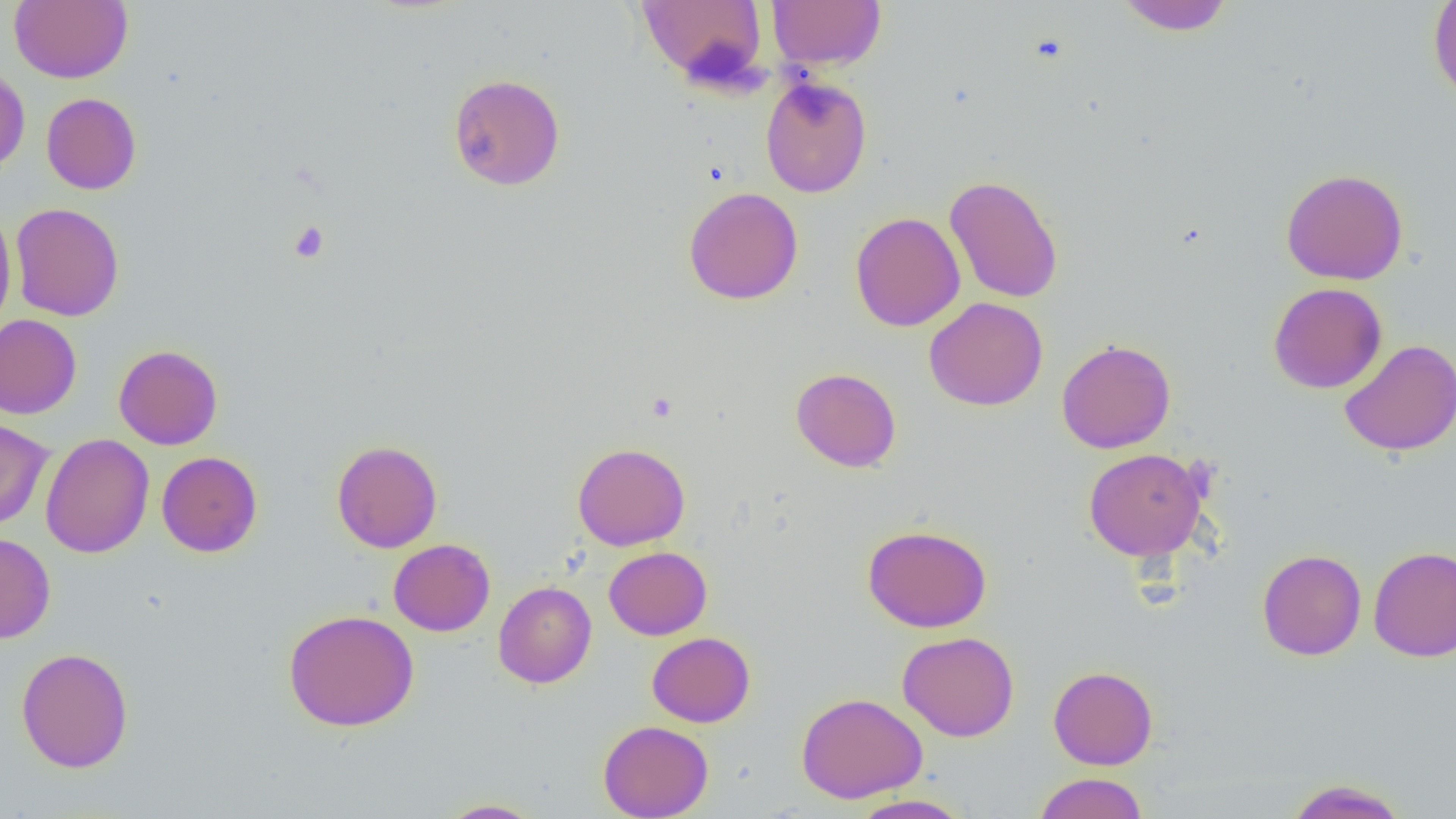
Summary:
  - Coordinate format: approximate bounding boxes as (x1,y1)-(x2,y2) corner pairs in pixels
  - Platelet locations: (289,221)-(329,263), (647,392)-(677,421)
  - Uninfected red blood cell locations: (10,0)-(132,83), (636,0)-(767,85), (767,0)-(886,71), (1115,0)-(1234,35), (1428,0)-(1456,103), (0,65)-(30,176), (447,73)-(565,190), (760,76)-(872,198), (41,92)-(142,194), (1281,168)-(1408,285), (944,174)-(1063,303), (683,186)-(803,305), (10,203)-(124,321), (0,206)-(16,334), (850,212)-(965,332), (1268,282)-(1387,394), (924,297)-(1048,411), (0,314)-(82,419), (1056,339)-(1175,454), (1338,339)-(1456,457), (113,344)-(223,450), (790,367)-(902,472), (0,418)-(53,530), (40,432)-(154,559), (331,439)-(442,553), (573,442)-(690,550), (1083,448)-(1208,562), (156,451)-(263,557), (862,525)-(992,633), (0,532)-(55,644), (388,538)-(495,636), (1368,546)-(1456,662), (604,547)-(712,640), (1257,549)-(1367,661), (493,581)-(597,688), (283,609)-(419,732), (647,631)-(756,727), (897,631)-(1020,742), (16,647)-(134,773), (1048,665)-(1158,770), (796,692)-(927,803), (598,720)-(713,819), (1033,772)-(1148,818), (1285,779)-(1410,819), (848,794)-(973,819), (436,798)-(545,818)
  - Slide-level diagnosis: negative for blood parasites
  - Modality: light microscopy
  - Field of view: single
  - Magnification: 1000x
  - Preparation: thin blood smear
  - Image size: 1456×819 pixels